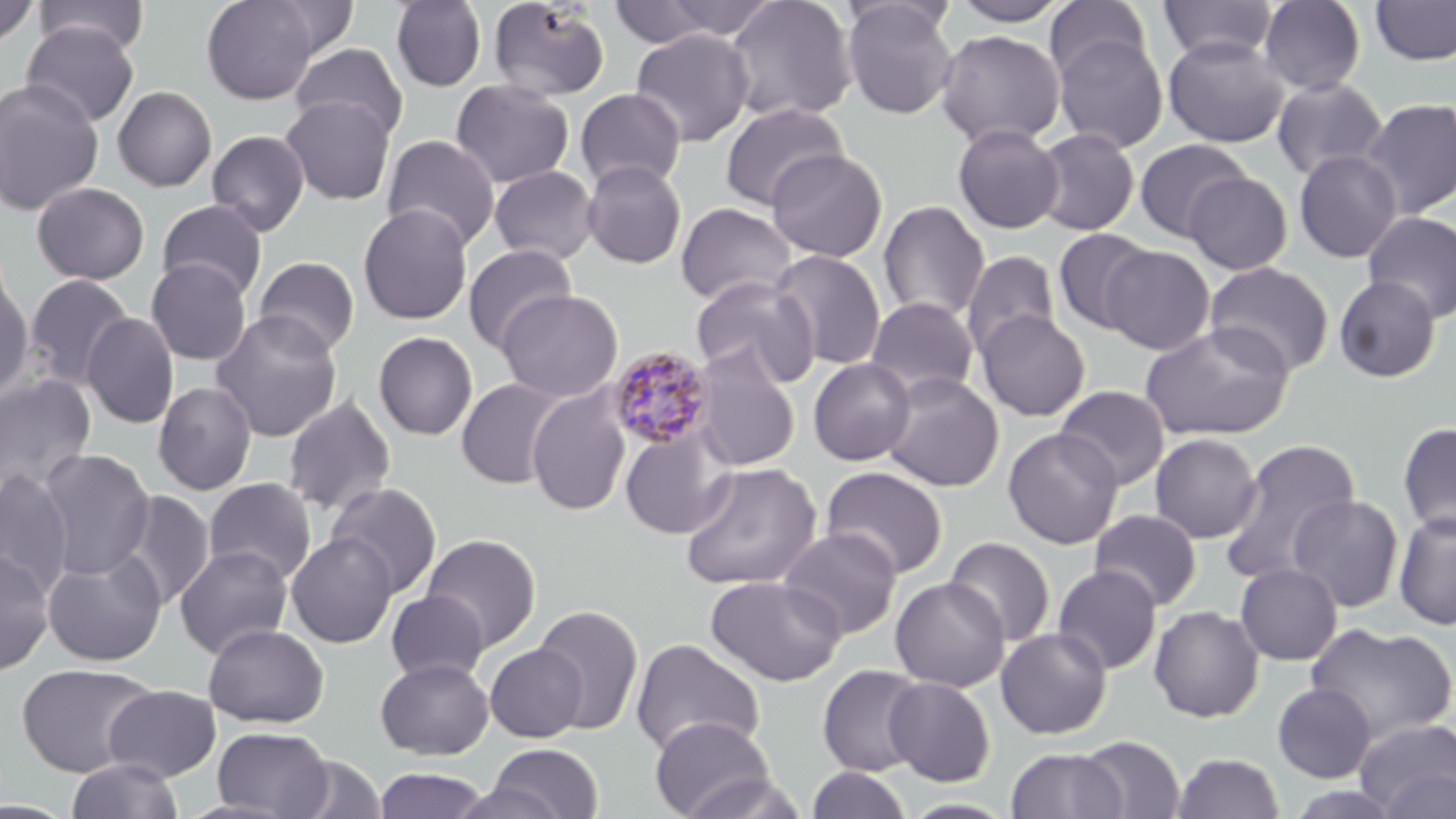

{
  "slide_level_diagnosis": "Plasmodium malariae",
  "preparation": "thin blood smear",
  "uninfected_red_blood_cell_locations": "approximate bounding boxes as (x1,y1)-(x2,y2) corner pairs in pixels: (33,0)-(150,56), (201,0)-(321,104), (391,0)-(487,92), (487,0)-(611,101), (722,0)-(858,123), (841,0)-(958,119), (1044,0)-(1151,84), (1157,0)-(1276,63), (1258,0)-(1366,95), (0,1)-(40,49), (258,1)-(359,60), (643,1)-(787,43), (949,1)-(1070,26), (1370,1)-(1456,66), (606,2)-(722,50), (21,22)-(139,128), (630,28)-(754,147), (935,29)-(1065,148), (1052,32)-(1168,153), (1163,35)-(1288,148), (290,43)-(409,142), (1271,76)-(1388,182), (0,77)-(104,216), (450,79)-(575,189), (112,85)-(217,192), (575,87)-(687,191), (280,95)-(396,205), (1360,98)-(1456,219), (719,102)-(849,211), (952,124)-(1064,234), (1032,128)-(1139,236), (206,129)-(310,237), (382,134)-(500,251), (1134,139)-(1251,243), (766,148)-(888,263), (1293,149)-(1403,263), (581,160)-(688,269), (489,165)-(600,265), (1183,171)-(1293,275), (31,181)-(150,285), (156,199)-(268,303), (878,200)-(990,323), (675,202)-(797,306), (358,204)-(473,325), (1362,211)-(1456,323), (1052,228)-(1156,335), (463,243)-(578,354), (1101,245)-(1215,354), (769,249)-(887,372), (961,251)-(1059,359), (254,256)-(360,357), (146,259)-(252,365), (1204,262)-(1335,377), (24,274)-(135,390), (1333,275)-(1441,383), (0,276)-(35,402), (690,276)-(818,387), (495,289)-(623,402), (865,297)-(980,400), (211,310)-(343,442), (976,310)-(1090,421), (82,313)-(179,429), (1140,322)-(1294,441), (373,331)-(478,440), (691,346)-(801,471), (808,357)-(916,466), (0,373)-(98,497), (881,373)-(1005,492), (456,378)-(567,490), (153,380)-(257,495), (1054,385)-(1170,490), (527,387)-(632,517), (282,394)-(397,516), (1397,421)-(1456,538), (620,423)-(737,540), (1003,427)-(1123,549), (1150,432)-(1262,544), (1220,441)-(1360,586), (37,448)-(156,580), (679,461)-(823,591), (820,466)-(949,578), (0,468)-(76,599), (203,477)-(317,586), (325,481)-(442,599), (115,491)-(214,610), (1287,494)-(1404,613), (1089,509)-(1202,611), (1393,511)-(1456,631), (778,527)-(902,640), (286,532)-(398,648), (421,533)-(542,652), (944,536)-(1055,646), (174,545)-(293,659), (42,548)-(166,667), (0,549)-(54,675), (1235,563)-(1343,665), (1052,565)-(1162,674), (706,574)-(845,686), (889,577)-(1010,692), (386,590)-(489,683), (532,604)-(644,734), (1148,605)-(1265,723), (1305,622)-(1455,745), (203,623)-(329,728), (996,627)-(1112,738), (630,637)-(765,759), (485,643)-(587,742), (375,658)-(494,759), (17,662)-(158,777), (817,664)-(928,776), (884,677)-(996,786), (1272,682)-(1377,783), (102,685)-(222,782), (650,716)-(775,819), (1353,718)-(1456,817), (213,726)-(333,818), (1075,735)-(1186,819), (484,743)-(605,819), (1005,747)-(1127,819), (1173,752)-(1285,818), (286,755)-(388,818), (66,757)-(183,819), (372,767)-(491,818), (806,767)-(911,819), (1378,769)-(1456,819), (676,771)-(809,819), (899,797)-(1019,818), (0,799)-(79,818), (174,799)-(300,819)",
  "stain": "May-Grünwald-Giemsa",
  "plasmodium_malariae_infected_red_blood_cell_locations": "approximate bounding boxes as (x1,y1)-(x2,y2) corner pairs in pixels: (608,345)-(714,450)",
  "field_of_view": "one of a larger specimen",
  "image_size": "1456×819 pixels",
  "modality": "light microscopy",
  "magnification": "1000x"
}